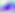
Summary:
  - Magnification: 400x
  - Modality: photomicrograph
  - Identification: Toxoplasma gondii